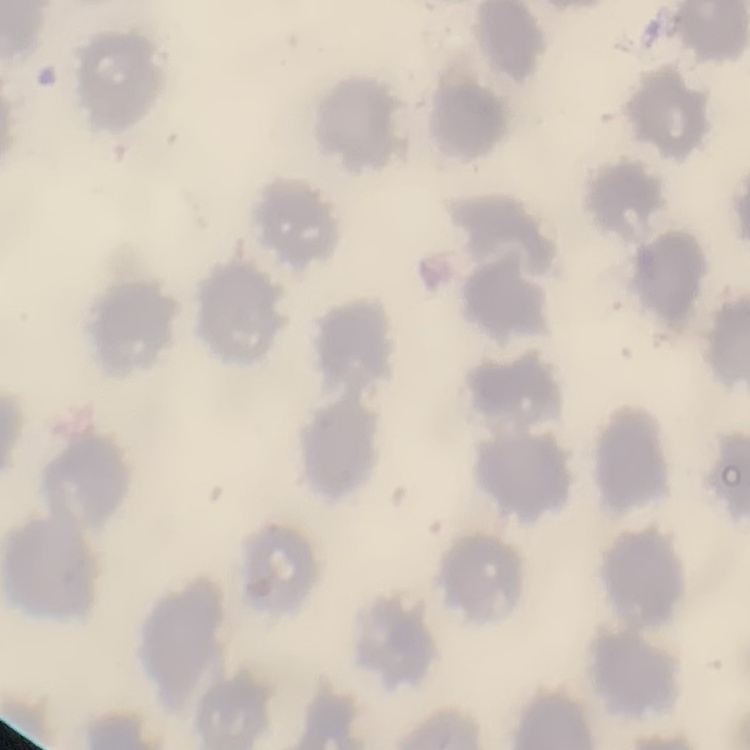

erythrocyte morphology = no rouleaux formation
image type = square crop of a larger photomicrograph
preparation = thin peripheral smear
stain = Field's or Giemsa